Locate every Plasmodium malariae-infected red blood cell.
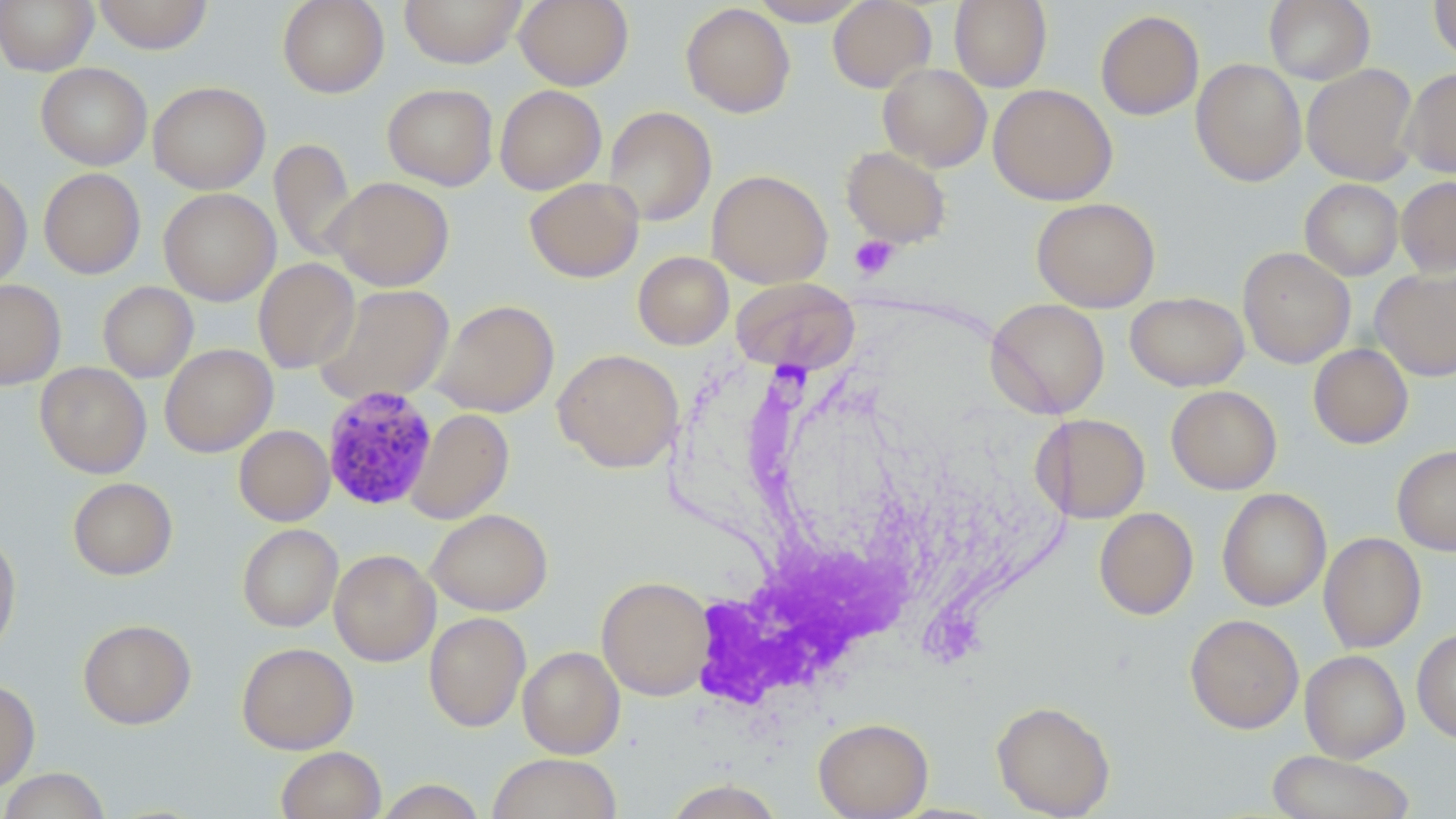
Approximate bounding boxes as (x1,y1)-(x2,y2) corner pairs in pixels.
Plasmodium malariae-infected red blood cells: (322,384)-(438,509).

Summary:
  - Uninfected red blood cell locations: (0,0)-(98,75), (93,0)-(213,54), (277,0)-(389,98), (399,0)-(527,67), (515,0)-(633,90), (748,0)-(870,25), (827,0)-(936,92), (949,0)-(1052,91), (1264,0)-(1375,85), (1428,1)-(1456,64), (680,3)-(795,118), (1095,10)-(1204,120), (1191,59)-(1306,186), (36,62)-(152,170), (878,63)-(991,171), (1302,64)-(1418,185), (1402,67)-(1456,178), (148,81)-(270,193), (383,83)-(498,190), (989,84)-(1117,205), (494,85)-(606,195), (603,106)-(717,226), (269,138)-(356,262), (841,146)-(952,249), (38,168)-(145,278), (0,169)-(32,289), (707,169)-(833,288), (326,176)-(454,291), (1396,176)-(1456,277), (524,177)-(644,282), (1300,179)-(1403,281), (159,188)-(280,306), (1032,198)-(1160,312), (1238,247)-(1355,368), (633,251)-(734,349), (253,258)-(360,374), (1371,269)-(1456,381), (731,278)-(860,373), (0,279)-(66,390), (98,281)-(198,383), (314,284)-(455,406), (1125,291)-(1249,391), (432,299)-(559,418), (985,299)-(1109,418), (160,343)-(277,458), (1308,343)-(1413,449), (553,348)-(683,473), (35,362)-(151,478), (1166,385)-(1282,494), (405,409)-(514,524), (1034,414)-(1151,523), (234,425)-(334,526), (1392,445)-(1456,556), (68,477)-(177,579), (1217,488)-(1331,611), (1094,507)-(1198,620), (427,509)-(552,615), (237,524)-(343,632), (0,532)-(21,659), (1318,532)-(1426,653), (329,549)-(440,666), (597,575)-(714,700), (424,611)-(531,732), (1185,614)-(1304,733), (77,619)-(197,729), (1411,627)-(1456,743), (236,642)-(358,754), (518,645)-(625,758), (1300,649)-(1410,762), (0,678)-(40,792), (991,700)-(1116,818), (813,717)-(933,818), (276,746)-(386,819), (1267,750)-(1415,819), (487,753)-(622,818), (1,768)-(111,819), (374,779)-(487,819), (662,780)-(786,818)
  - Platelet locations: (849,235)-(898,281)
  - Slide-level diagnosis: Plasmodium malariae
  - Magnification: 1000x
  - Stain: May-Grünwald-Giemsa
  - Modality: optical microscopy
  - Image size: 1456×819 pixels
  - Field of view: single
  - Preparation: thin blood film